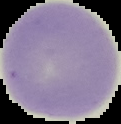 Image is 121×124 pixels. From a thin blood smear. Cell region segmented out of the field of view; the surrounding area is masked to black. Malaria status: uninfected.